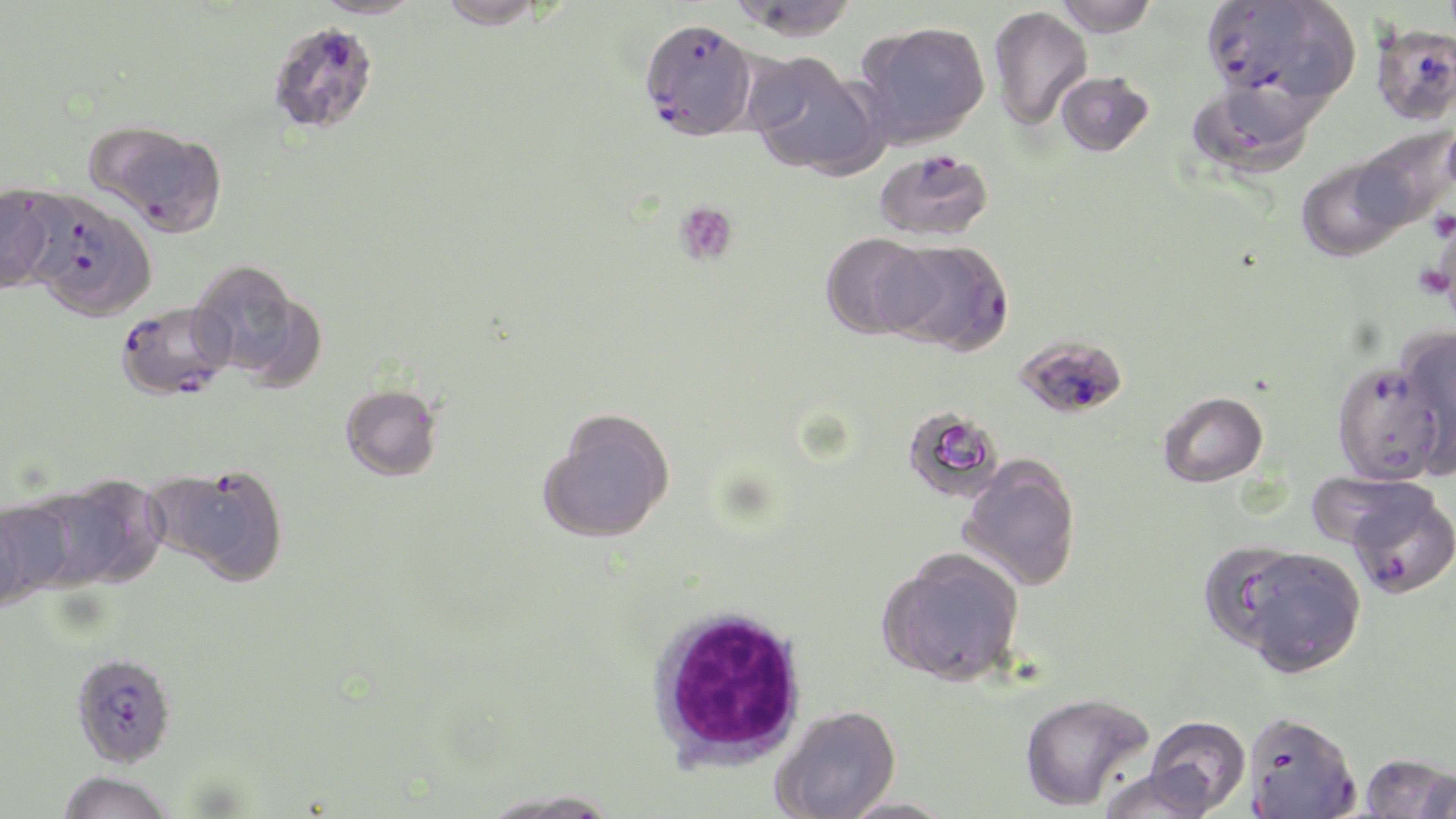

slide-level diagnosis = Plasmodium falciparum
modality = optical microscopy
platelet locations = approximate bounding boxes as (x1, y1, x2, y2) in pixels: (674, 201, 739, 266), (1428, 209, 1456, 242)
field of view = single
stain = May-Grünwald-Giemsa
preparation = thin blood smear
image size = 1456×819 pixels
magnification = 1000x
uninfected red blood cell locations = approximate bounding boxes as (x1, y1, x2, y2) in pixels: (312, 0, 424, 19), (435, 0, 550, 29), (727, 0, 860, 42), (1055, 0, 1158, 36), (1281, 0, 1360, 100), (988, 6, 1092, 131), (855, 20, 991, 148), (745, 52, 885, 179), (1055, 71, 1154, 157), (1190, 78, 1323, 180), (90, 122, 228, 237), (1351, 129, 1455, 232), (1294, 157, 1410, 261), (0, 184, 61, 294), (820, 232, 936, 339), (188, 259, 312, 382), (1395, 327, 1456, 476), (340, 384, 442, 481), (1158, 391, 1268, 487), (539, 409, 675, 544), (904, 409, 1008, 497), (958, 456, 1082, 591), (30, 476, 163, 591), (0, 497, 75, 601), (1215, 544, 1367, 675), (878, 547, 1025, 686), (1019, 691, 1155, 812), (770, 704, 902, 819), (1242, 712, 1360, 818), (1145, 716, 1250, 815), (1358, 752, 1454, 818), (1097, 767, 1218, 819), (54, 772, 174, 819), (475, 789, 626, 819), (834, 796, 961, 819)
Plasmodium falciparum-infected red blood cell locations = approximate bounding boxes as (x1, y1, x2, y2) in pixels: (1201, 0, 1298, 101), (638, 18, 759, 141), (266, 21, 379, 135), (1371, 23, 1456, 126), (874, 149, 993, 242), (25, 193, 156, 322), (926, 239, 1016, 356), (115, 302, 234, 401), (1015, 334, 1128, 419), (1330, 359, 1448, 485), (193, 465, 288, 585), (1344, 482, 1456, 600), (70, 652, 177, 768)
white blood cell locations = approximate bounding boxes as (x1, y1, x2, y2) in pixels: (646, 604, 810, 770)